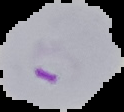

Result: Plasmodium parasites identified. Image is 124×112 pixels. Segmented cell region on a black background. From a thin blood smear.